Point out each Plasmodium parasite.
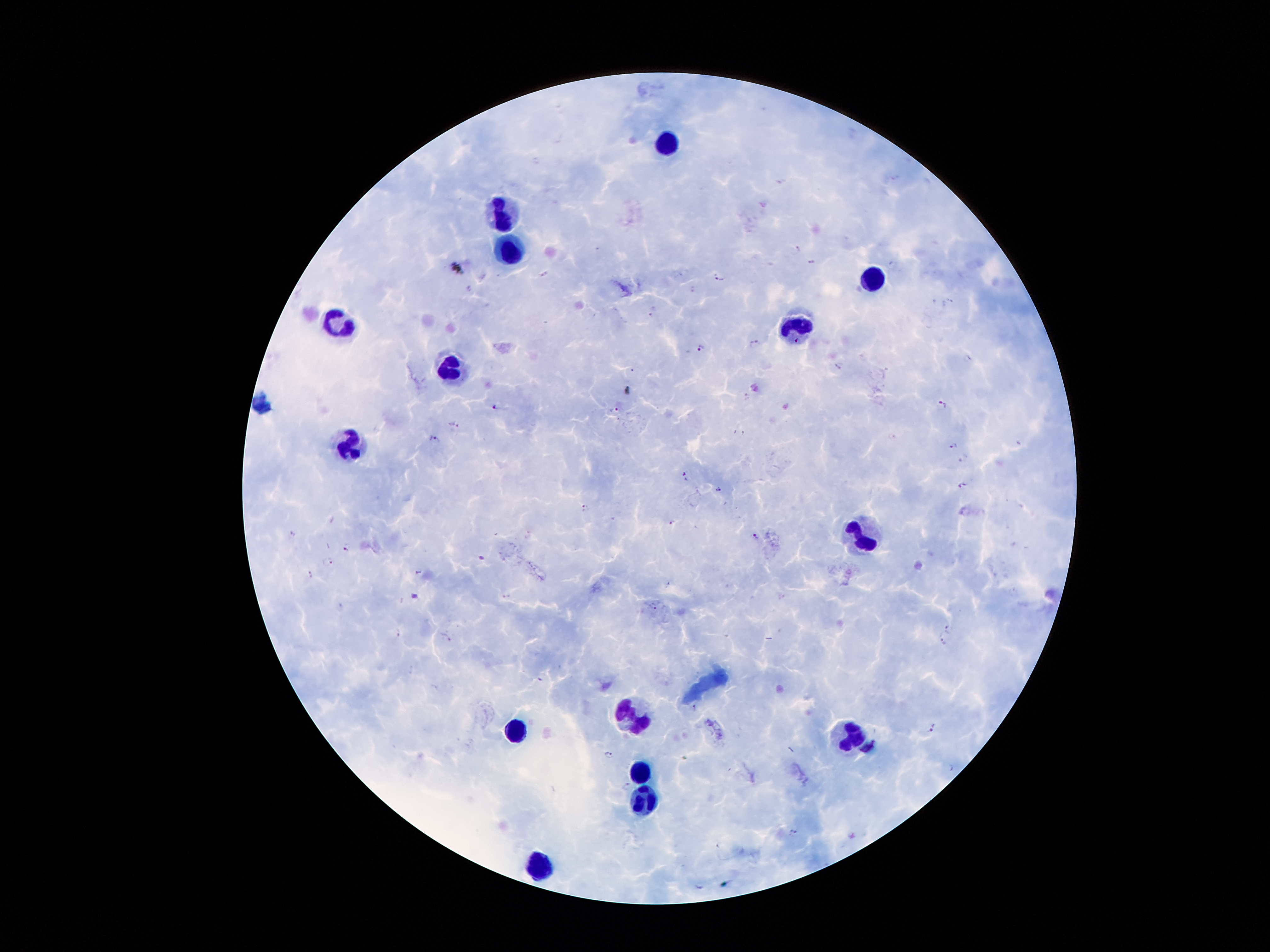

Approximate centers as [x, y] in pixels.
Plasmodium parasites: [797, 246], [811, 262], [890, 262], [456, 267], [545, 272], [718, 276], [468, 287], [693, 288], [949, 299], [934, 300], [652, 311], [753, 344], [700, 347], [968, 355], [837, 367], [633, 370], [627, 390], [746, 396], [942, 405], [496, 406], [614, 408], [453, 422], [434, 438], [952, 445], [963, 457], [685, 475], [962, 484], [719, 488], [585, 507], [965, 512], [672, 521], [291, 534], [755, 536], [346, 546], [481, 557], [328, 561], [418, 570], [309, 573], [339, 606], [653, 606], [950, 628], [397, 633], [447, 637], [942, 640], [695, 705], [932, 728], [609, 754], [949, 767], [626, 784], [793, 833].

leukocyte locations = [667, 146], [503, 213], [513, 251], [870, 280], [337, 323], [796, 326], [451, 367], [348, 447], [855, 534], [633, 717], [517, 730], [852, 735], [640, 771], [644, 801], [540, 865]
image size = 1270×952 pixels
magnification = 100x
patient malaria status = infected with Plasmodium falciparum
preparation = thick peripheral-blood smear
stain = Giemsa
capture = smartphone camera through the microscope eyepiece
field of view = one from this slide